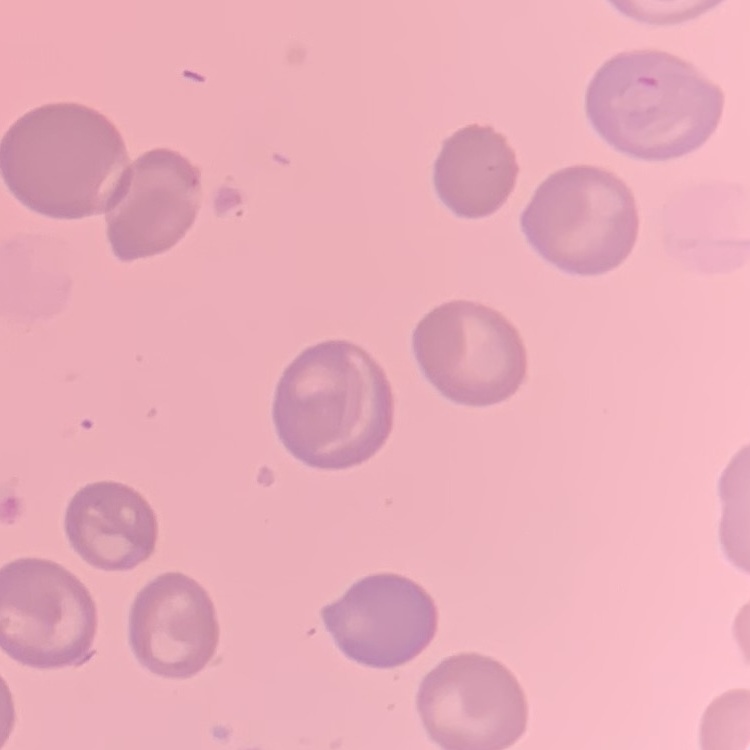

Summary:
  - Red blood cell morphology: no rouleaux formation
  - Image type: one tile cut from a larger photomicrograph
  - Stain: Field's or Giemsa
  - Preparation: thin blood smear